Classify this cell by malaria status.
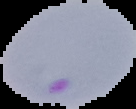

Parasitized.

Segmented cell region on a black background. From a thin blood smear. Image is 136×109 pixels.